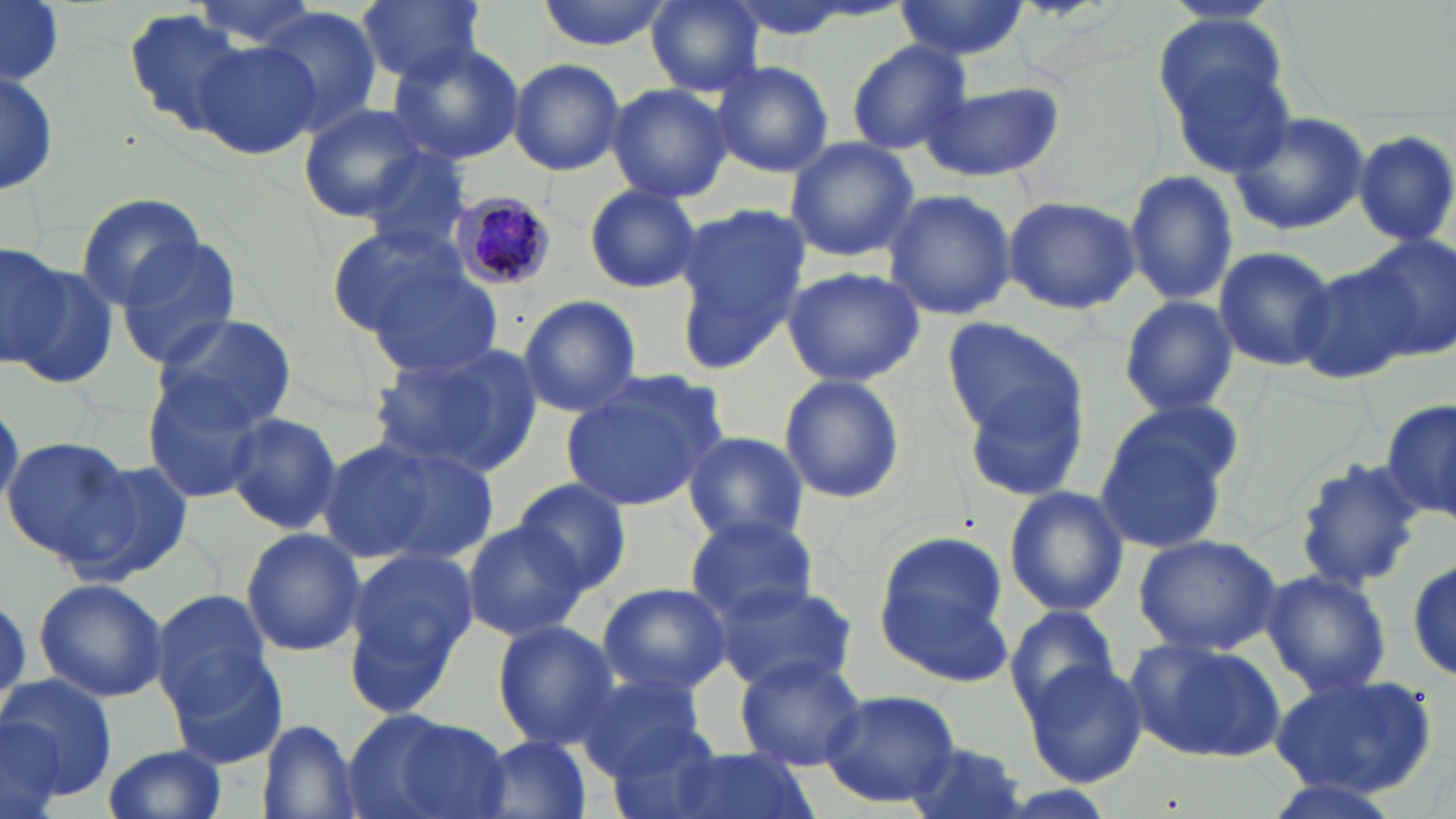
Approximate bounding boxes as (x1,y1)-(x2,y2) corner pairs in pixels. Plasmodium malariae-infected red blood cell locations: (453,192)-(560,291). Uninfected red blood cell locations: (0,0)-(68,83), (2,0)-(64,85), (355,0)-(486,84), (533,0)-(672,50), (645,0)-(762,96), (891,0)-(1030,60), (120,8)-(261,140), (257,8)-(384,136), (1159,19)-(1294,171), (194,39)-(321,160), (843,39)-(974,154), (387,41)-(525,168), (509,59)-(625,175), (1,62)-(58,202), (712,62)-(834,177), (914,79)-(1065,185), (607,82)-(734,206), (296,103)-(435,226), (1229,110)-(1370,237), (1353,130)-(1456,247), (783,136)-(920,262), (356,148)-(476,258), (1125,168)-(1238,310), (585,183)-(703,294), (881,189)-(1017,321), (76,192)-(206,310), (1002,192)-(1142,315), (670,206)-(809,369), (327,222)-(486,356), (1357,234)-(1455,360), (0,238)-(71,375), (114,238)-(244,370), (1211,245)-(1337,373), (5,260)-(118,391), (1293,260)-(1426,387), (364,263)-(506,382), (781,266)-(925,388), (516,295)-(643,418), (1118,295)-(1239,418), (150,313)-(297,430), (940,317)-(1091,441), (368,345)-(539,477), (777,374)-(908,505), (957,374)-(1092,505), (559,375)-(723,512), (142,377)-(269,502), (1383,395)-(1454,530), (1094,399)-(1243,548), (222,412)-(342,534), (682,432)-(810,547), (3,436)-(133,564), (332,436)-(502,569), (1291,457)-(1430,592), (68,460)-(194,585), (514,479)-(631,597), (1003,486)-(1129,616), (685,514)-(819,625), (461,519)-(589,642), (240,529)-(368,656), (875,532)-(1017,681), (1134,532)-(1285,656), (337,546)-(480,719), (1409,558)-(1456,681), (1260,569)-(1393,699), (34,576)-(167,703), (712,580)-(858,693), (596,582)-(733,697), (150,589)-(276,718), (1004,604)-(1122,718), (491,620)-(621,751), (1124,634)-(1291,763), (165,645)-(287,769), (735,656)-(866,769), (1022,658)-(1147,787), (574,670)-(708,777), (1269,671)-(1439,799), (2,673)-(116,806), (818,687)-(961,808), (343,708)-(510,819), (0,717)-(66,818), (258,721)-(362,819), (601,724)-(729,819), (477,735)-(595,819), (901,742)-(1032,819), (102,743)-(228,819), (659,744)-(815,819). Slide-level diagnosis: Plasmodium malariae. Captured at 1000x magnification. May-Grünwald-Giemsa stain. Single field of view. Image is 1456×819 pixels. Thin blood film. Optical microscopy.